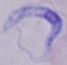

Summary:
  - Identification: trypanosome
  - Modality: micrograph
  - Magnification: 1000x